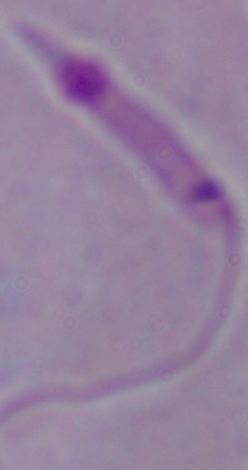
Summary:
  - Identification: Leishmania
  - Magnification: 1000x
  - Modality: micrograph